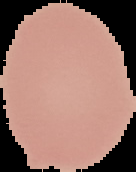

From a thin blood smear. Cell region segmented out of the field of view; the surrounding area is masked to black. Image is 136×172 pixels. Malaria status: uninfected.